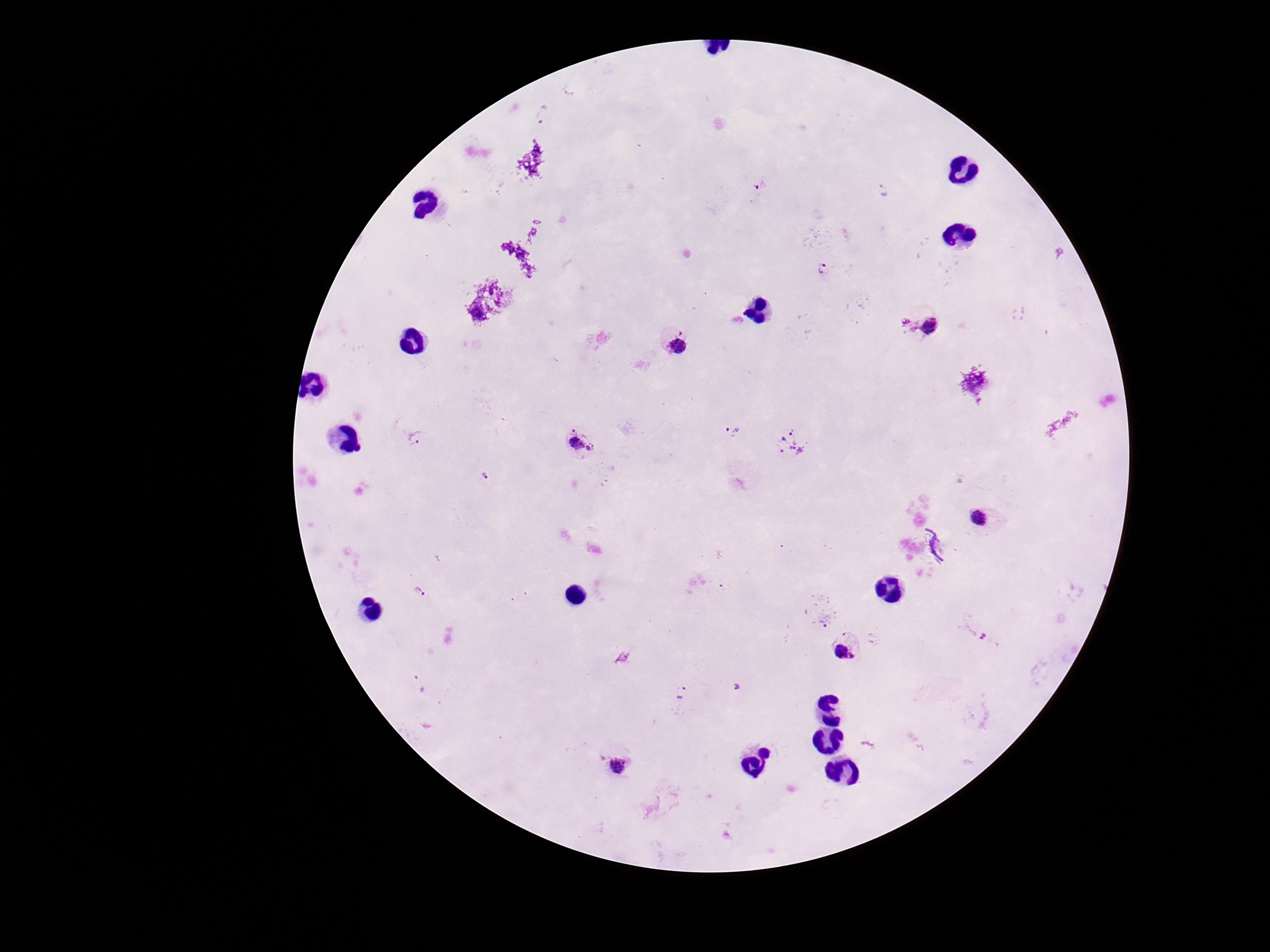 Approximate centers as [x, y] in pixels. Plasmodium parasite locations: [541, 117], [761, 183], [885, 190], [823, 269], [922, 327], [677, 344], [732, 431], [415, 438], [580, 444], [792, 444], [485, 475], [979, 519], [419, 592], [822, 619], [977, 634], [845, 651], [419, 684], [683, 694], [617, 766]. Smartphone photograph taken through the microscope eyepiece. Giemsa stain. Single field of view. Image is 1270×952 pixels. Thick peripheral-blood smear. 100x magnification. Patient malaria status: infected.